State which parasite is depicted.
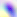

Toxoplasma gondii.

Summary:
  - Magnification: 400x
  - Modality: micrograph